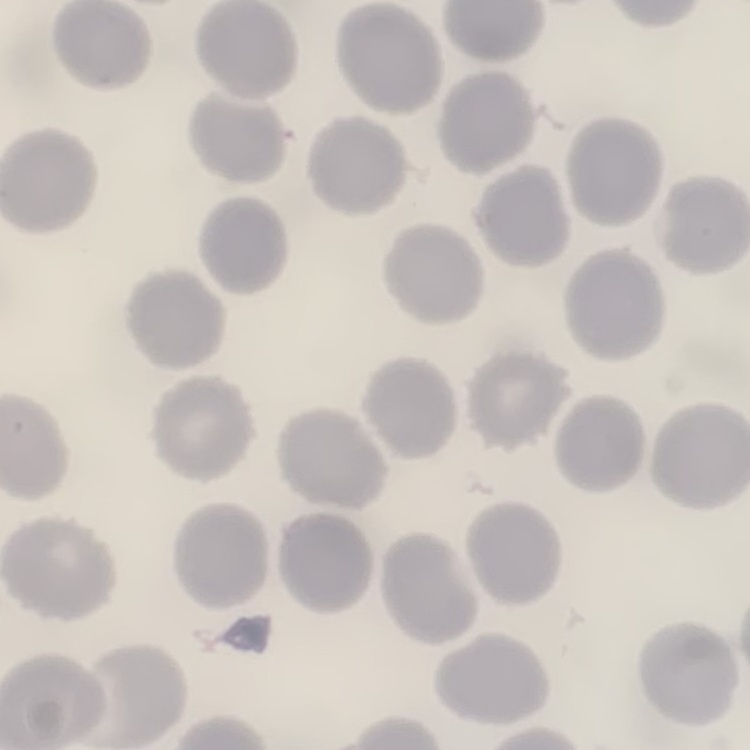 The red blood cells show no rouleaux formation. One tile cut from a larger photomicrograph. Field's or Giemsa stain. Thin blood smear.